Describe the morphology of the erythrocytes.
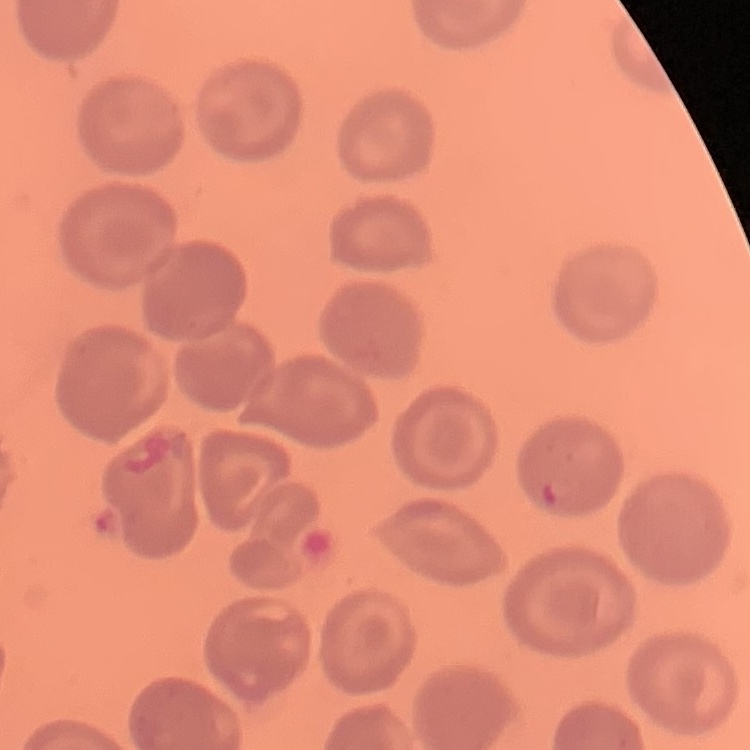
They show no rouleaux formation.

Stained with either Field's or Giemsa. Thin peripheral smear. One tile cut from a larger photomicrograph.